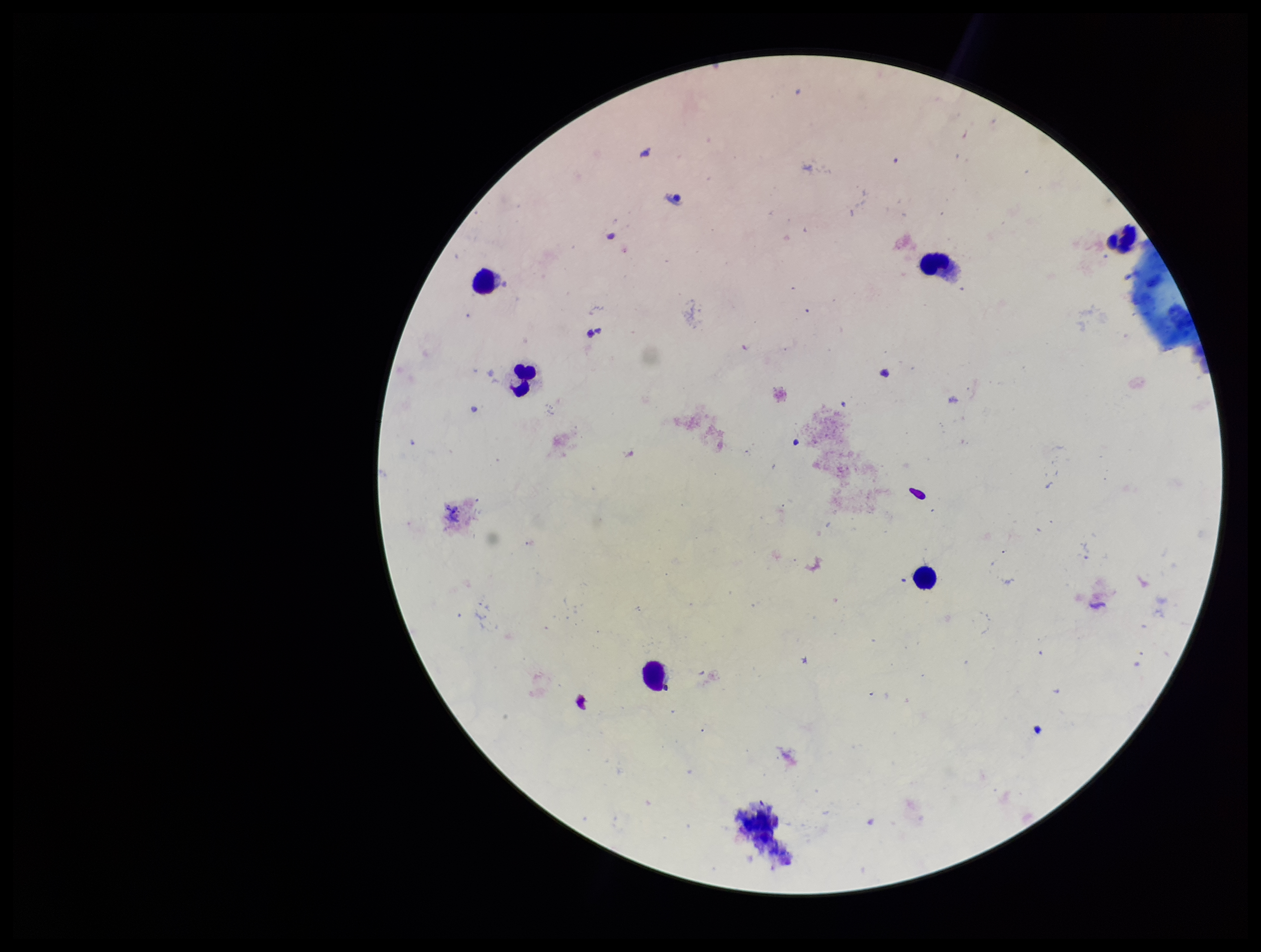

Summary:
  - Parasite count: 0
  - Leukocyte count: 6
  - Capture: smartphone photograph through the microscope eyepiece
  - Plasmodium parasites: none seen
  - Preparation: thick blood smear
  - Image size: 1261×952 pixels
  - Stain: Giemsa
  - Patient malaria status: negative
  - Field of view: single